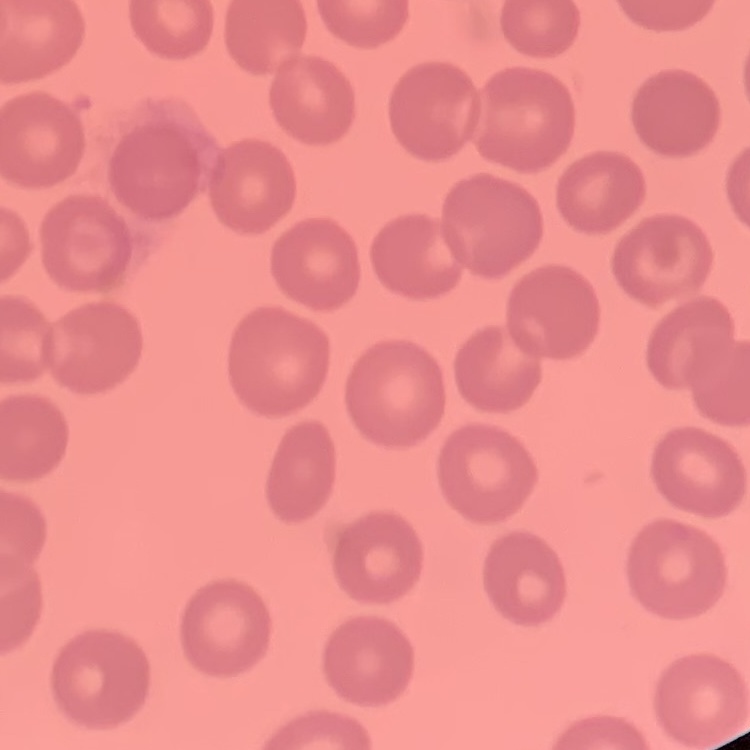

{
  "erythrocyte_morphology": "no rouleaux formation",
  "preparation": "thin blood film",
  "image_type": "one tile cut from a larger photomicrograph",
  "stain": "Field's or Giemsa"
}